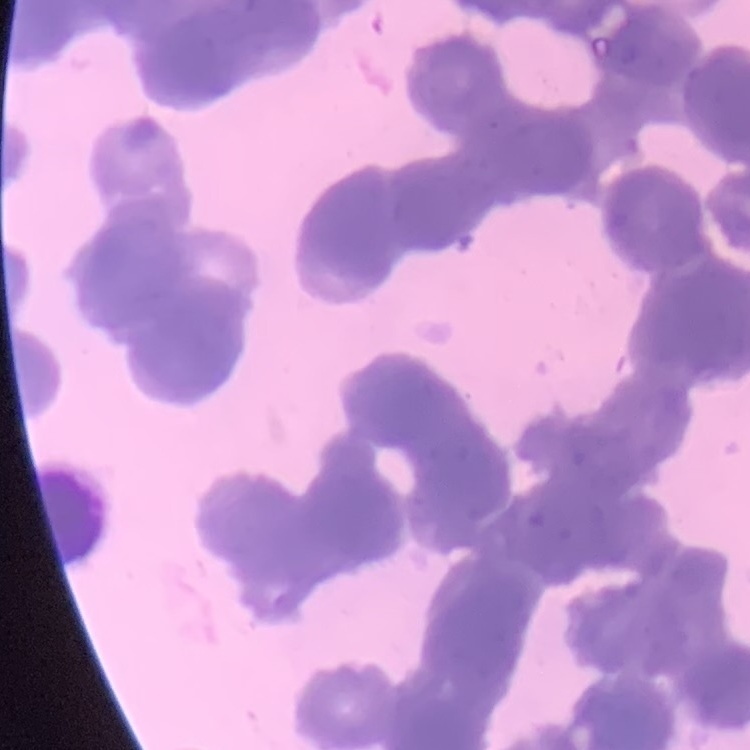
red blood cell morphology = rouleaux formation
stain = Field's or Giemsa
preparation = thin blood film
image type = one tile cut from a larger photomicrograph